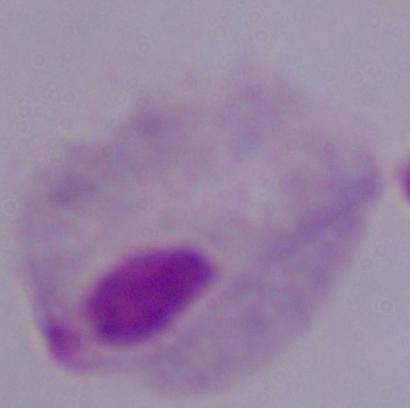 Captured at 1000x magnification. A trichomonad is shown. Photomicrograph.